Identify the malaria species.
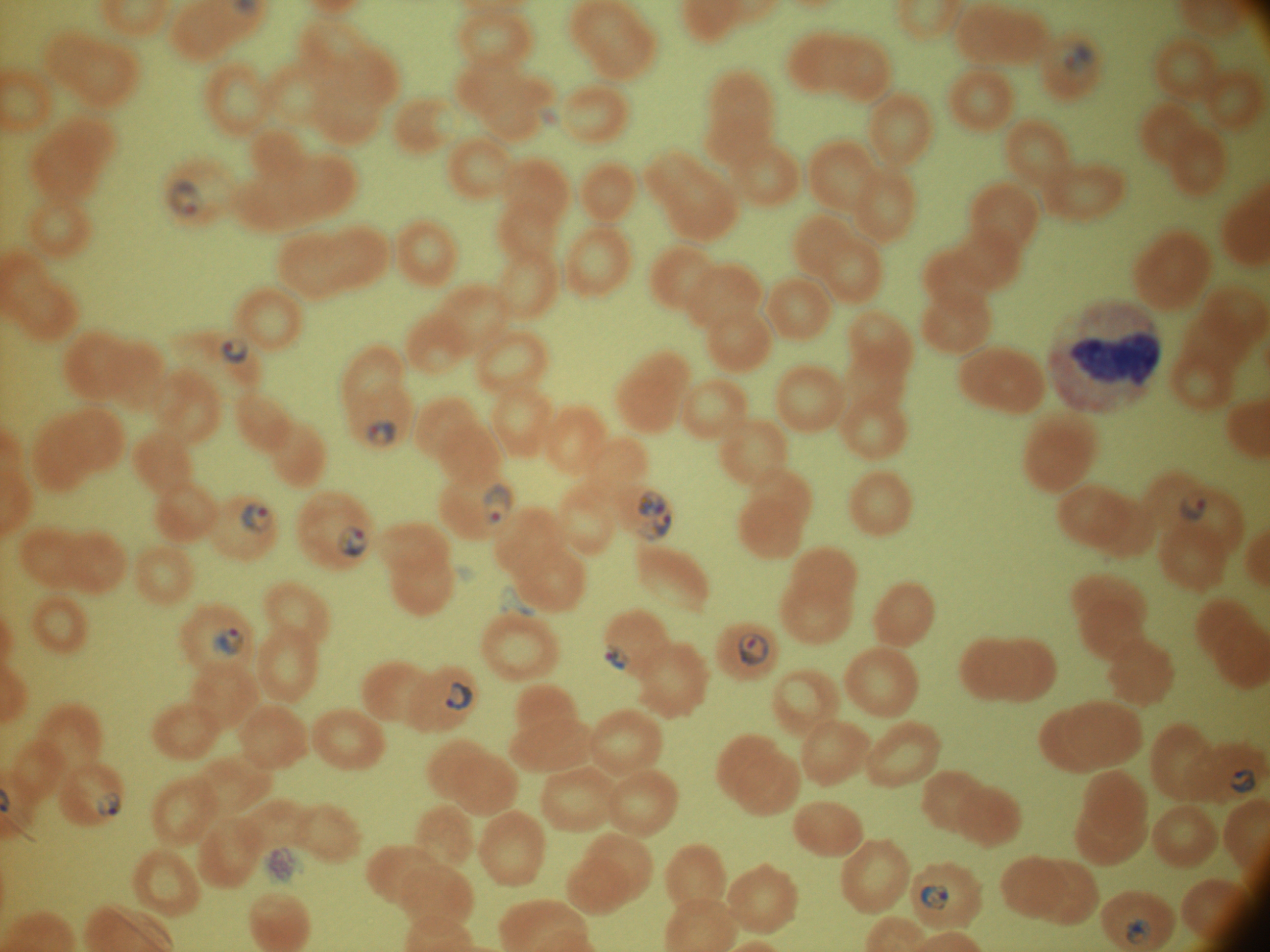

Plasmodium falciparum.

Approximate bounding boxes as (x1, y1, x2, y2) in pixels, from the source annotation, which is not necessarily exhaustive. Ring form locations: (1063, 42, 1095, 74), (169, 180, 201, 215), (221, 337, 249, 364), (366, 420, 396, 447), (483, 482, 512, 526), (636, 490, 667, 518), (1179, 491, 1207, 521), (241, 502, 274, 534), (636, 509, 673, 540), (337, 525, 369, 559), (212, 627, 244, 658), (737, 632, 769, 666), (605, 643, 630, 671), (446, 682, 473, 711), (1230, 769, 1256, 793), (97, 792, 121, 817), (919, 883, 951, 912), (1125, 917, 1150, 944). One field from this slide. Captured at 100x magnification. Giemsa-stained preparation. Image is 1270×952 pixels. Leica DM2000 optical microscope with a built-in camera. Thin blood smear.